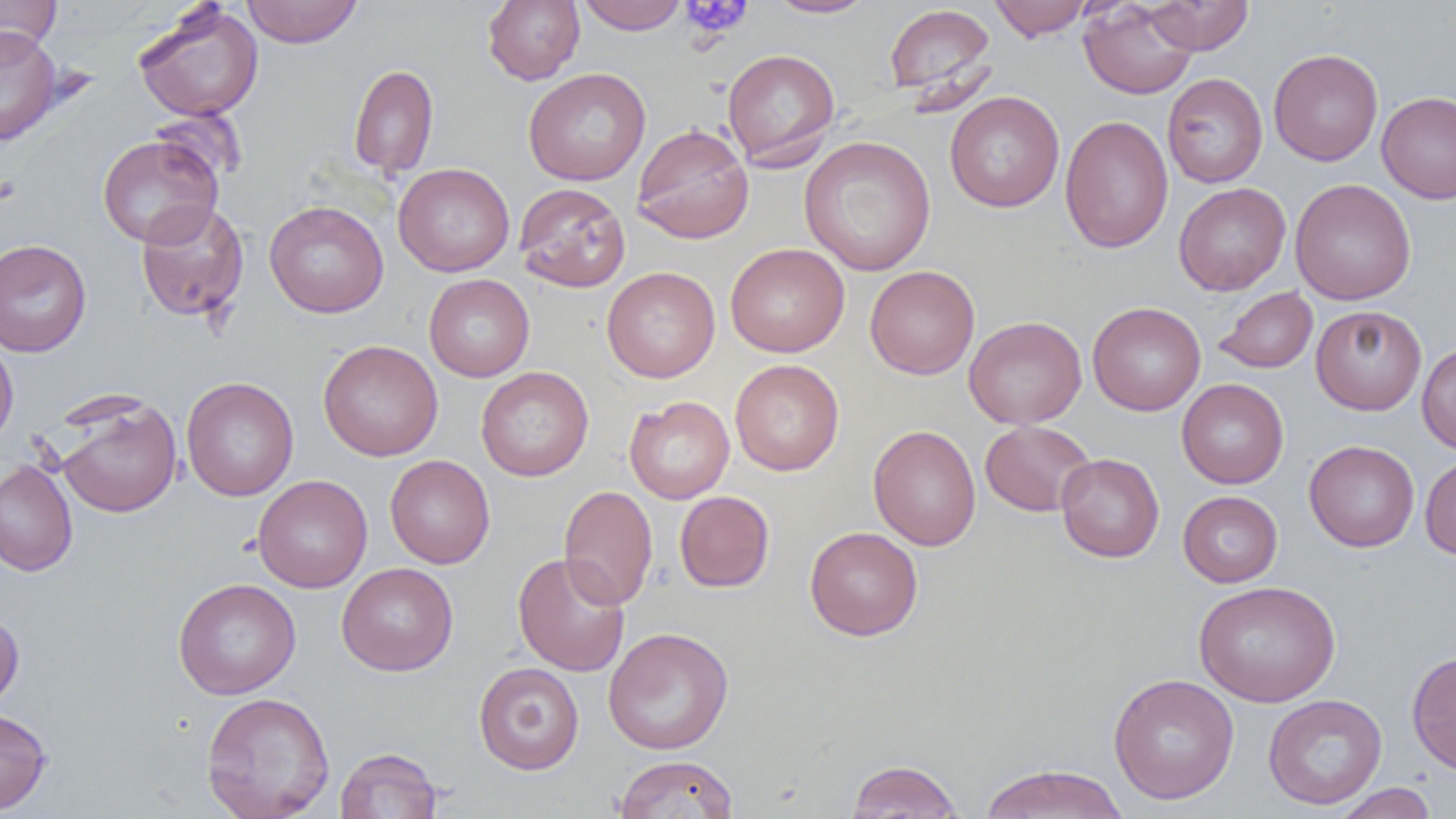

Approximate bounding boxes as (x1, y1, x2, y2) in pixels. Uninfected red blood cell locations: (0, 0, 61, 57), (241, 0, 363, 48), (482, 0, 585, 85), (577, 0, 689, 34), (765, 0, 879, 18), (989, 0, 1092, 40), (1142, 0, 1255, 55), (1079, 1, 1198, 99), (132, 3, 264, 122), (883, 3, 996, 101), (0, 26, 62, 146), (722, 48, 840, 169), (1269, 48, 1383, 166), (348, 63, 439, 180), (522, 67, 651, 186), (1162, 72, 1267, 188), (944, 91, 1064, 213), (1377, 91, 1456, 204), (149, 107, 246, 188), (1060, 115, 1174, 253), (632, 123, 754, 244), (97, 133, 223, 248), (798, 135, 937, 276), (393, 162, 515, 277), (1290, 178, 1416, 305), (514, 182, 631, 293), (1173, 182, 1291, 296), (264, 200, 389, 317), (135, 201, 249, 322), (0, 239, 92, 357), (725, 243, 850, 357), (864, 265, 980, 379), (602, 266, 720, 382), (424, 274, 535, 382), (1213, 286, 1318, 374), (1087, 301, 1205, 416), (1311, 305, 1427, 415), (963, 316, 1087, 429), (0, 335, 18, 447), (318, 339, 444, 461), (1416, 341, 1456, 454), (730, 359, 844, 476), (476, 366, 594, 482), (181, 377, 299, 500), (1177, 378, 1289, 489), (55, 395, 182, 519), (624, 396, 735, 504), (979, 420, 1097, 517), (868, 425, 981, 551), (1304, 440, 1420, 552), (1056, 453, 1164, 562), (1420, 454, 1456, 560), (385, 455, 495, 569), (0, 459, 78, 576), (253, 475, 372, 593), (558, 485, 658, 611), (674, 491, 775, 592), (1178, 491, 1283, 587), (804, 526, 923, 641), (513, 553, 630, 677), (336, 562, 458, 676), (172, 577, 301, 700), (1194, 580, 1340, 706), (0, 610, 24, 712), (603, 627, 734, 755), (1407, 650, 1456, 776), (474, 662, 584, 774), (1107, 673, 1239, 805), (201, 691, 335, 819), (1262, 694, 1387, 810), (0, 708, 52, 815), (335, 747, 442, 818), (614, 754, 739, 818), (845, 759, 964, 818), (977, 763, 1128, 818), (1331, 783, 1438, 819). Platelet locations: (680, 0, 752, 39), (0, 173, 21, 205). Slide-level diagnosis: negative for blood parasites. Image is 1456×819 pixels. Captured at 1000x magnification. Single field of view. Light microscopy. Thin blood film.